Give the position of every Plasmodium parasite.
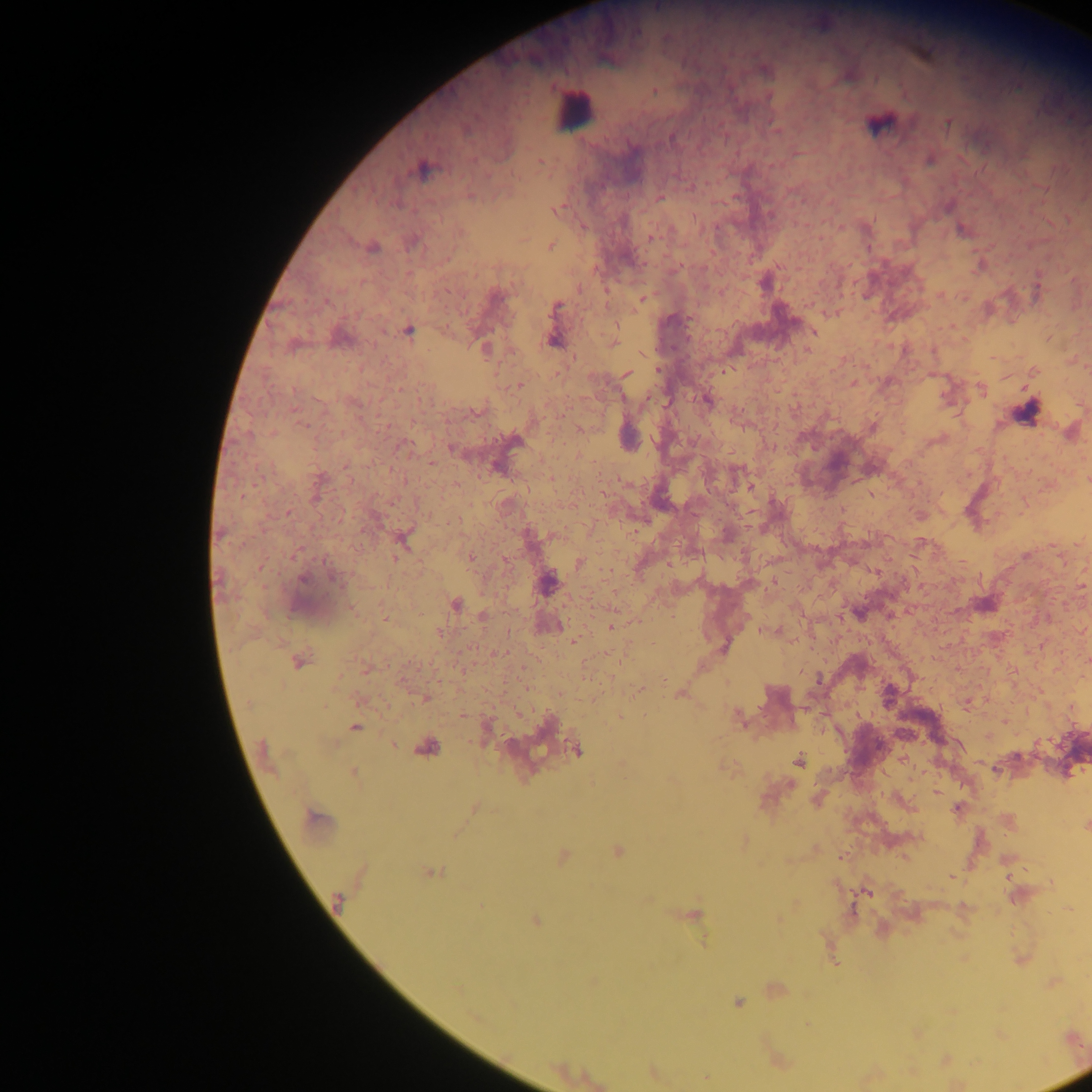

Approximate centers as [x, y] in pixels.
Plasmodium parasites: [947, 124], [672, 138], [930, 161], [541, 163], [421, 169], [659, 198], [948, 206], [557, 210], [961, 228], [652, 238], [551, 246], [373, 248], [980, 267], [764, 283], [495, 296], [642, 299], [555, 307], [409, 331], [813, 331], [554, 340], [613, 343], [485, 349], [807, 349], [658, 369], [626, 374], [853, 383], [519, 385], [981, 390], [707, 401], [301, 424], [873, 427], [581, 428], [514, 440], [452, 449], [431, 464], [750, 487], [288, 513], [403, 539], [920, 542], [1027, 555], [471, 558], [579, 563], [304, 579], [333, 579], [547, 583], [1081, 586], [985, 604], [455, 605], [859, 613], [483, 615], [385, 617], [611, 626], [573, 640], [724, 647], [299, 661], [1087, 661], [817, 680], [638, 690], [888, 694], [425, 699], [620, 716], [740, 718], [355, 727], [393, 745], [426, 749], [576, 750], [798, 761], [353, 774], [937, 792], [474, 808], [957, 809], [315, 819], [1086, 826], [618, 851], [564, 856], [843, 857], [433, 873], [951, 877], [867, 893], [337, 900], [695, 915], [535, 920], [704, 941], [835, 963], [738, 1002], [707, 1078].

Summary:
  - Leukocyte locations: [575, 112]
  - Image size: 1092×1092 pixels
  - Country: Ghana
  - Capture: mobile-phone photograph through a microscope
  - Preparation: thick blood film
  - Field of view: single